Assess this cell for malaria.
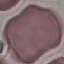

Uninfected.

capture: smartphone through the microscope eyepiece
preparation: thin blood smear
image_type: automatically extracted cell patch, resized to 64 × 64 pixels
stain: Giemsa